Name the cell type shown.
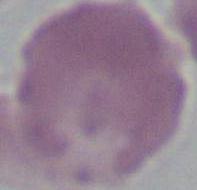

This is an erythrocyte.

{
  "magnification": "1000x",
  "modality": "photomicrograph"
}